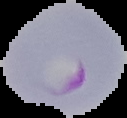 Cell region segmented out of the field of view; the surrounding area is masked to black. From a thin blood film. Image is 127×118 pixels. Malaria status: parasitized.